Comment on the morphology of the erythrocytes.
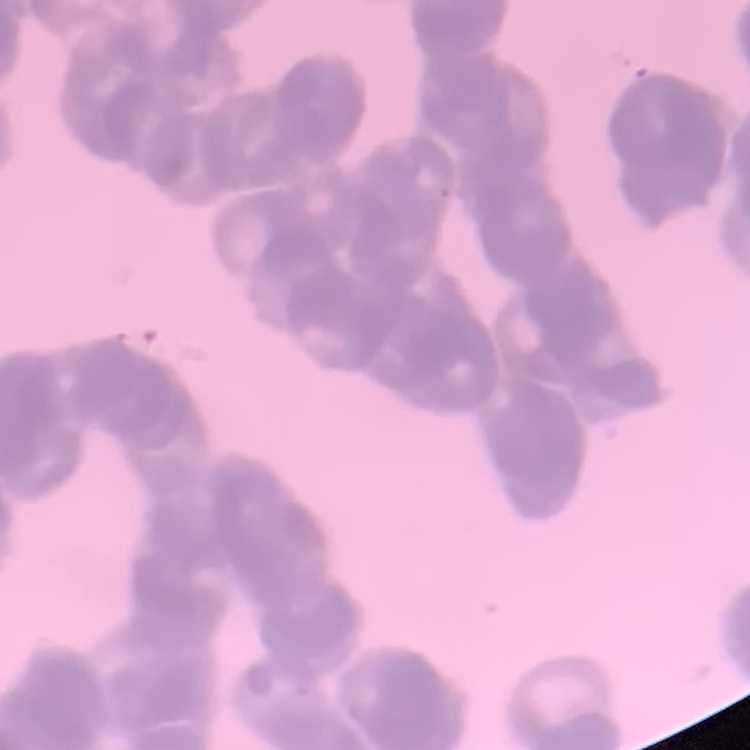
They show rouleaux formation.

Thin peripheral smear. Field's or Giemsa stain. One tile cut from a larger photomicrograph.